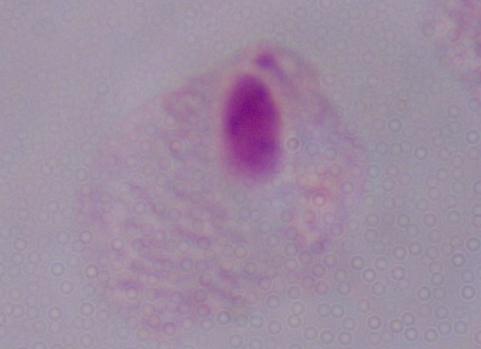
Photomicrograph. A trichomonad is seen. 1000x magnification.